Locate every blood parasite and identify its species.
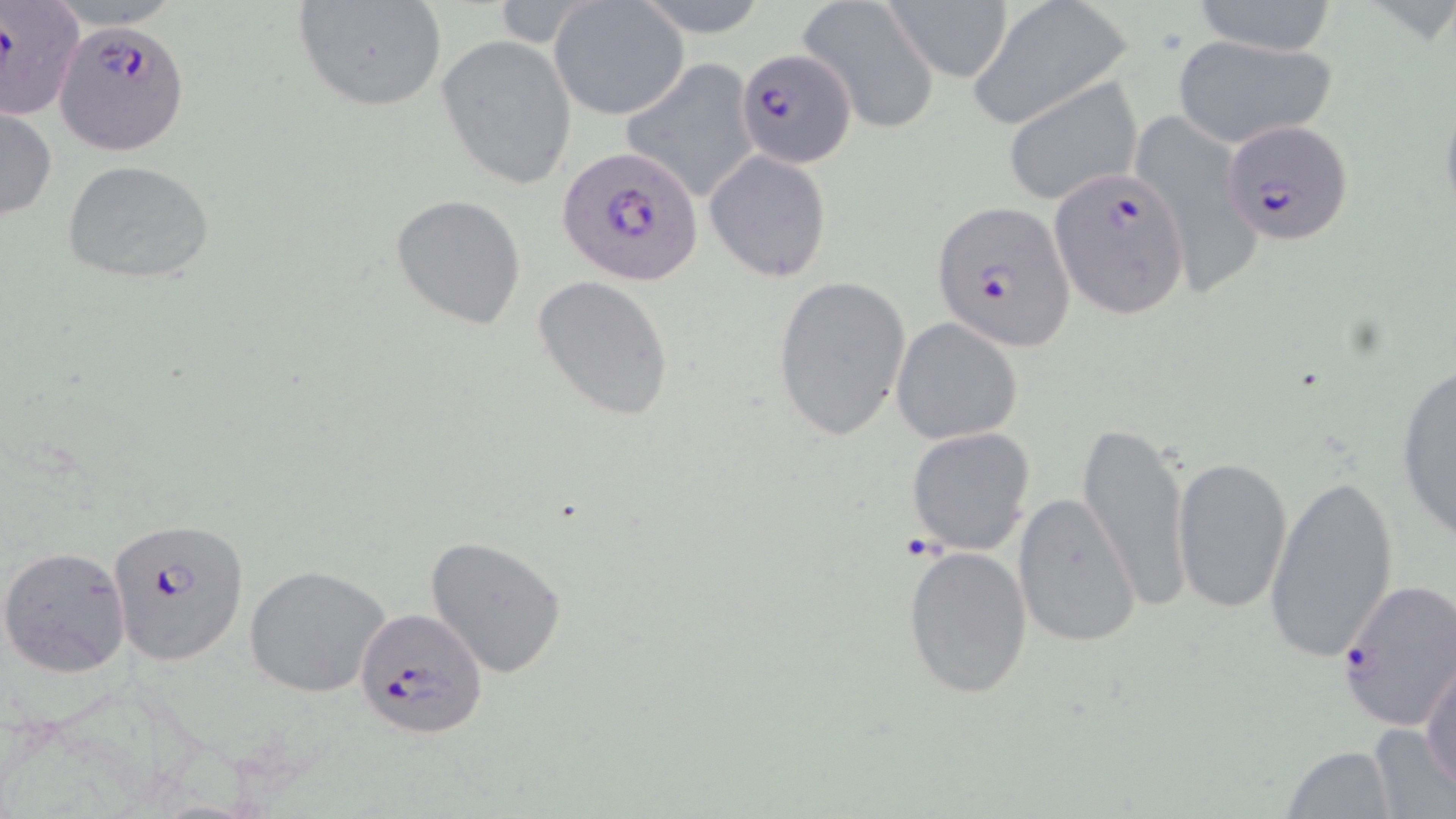

Approximate bounding boxes as (x1,y1)-(x2,y2) corner pairs in pixels.
Plasmodium falciparum-infected red blood cells: (0,3)-(80,121), (54,20)-(190,155), (736,47)-(857,168), (1222,121)-(1355,246), (557,146)-(702,284), (1046,166)-(1189,320), (930,203)-(1075,350), (107,516)-(247,664), (1336,579)-(1456,732), (353,607)-(488,738).
No Plasmodium ovale, Plasmodium malariae, Plasmodium vivax, Babesia divergens, or Trypanosoma brucei observed.

Uninfected red blood cell locations: (292,0)-(449,113), (633,0)-(773,39), (798,0)-(941,134), (883,0)-(1014,83), (549,1)-(687,121), (1187,1)-(1341,56), (972,2)-(1132,124), (438,33)-(576,189), (1171,35)-(1338,148), (621,57)-(760,203), (1001,77)-(1144,206), (0,105)-(56,222), (1125,107)-(1265,291), (703,150)-(834,284), (62,158)-(215,285), (390,193)-(527,330), (772,274)-(912,441), (534,275)-(675,420), (889,317)-(1024,445), (1394,359)-(1456,544), (1077,421)-(1192,611), (906,428)-(1036,555), (1171,455)-(1292,614), (1265,472)-(1398,662), (1012,491)-(1142,649), (425,535)-(568,679), (903,544)-(1033,699), (0,545)-(131,678), (244,564)-(393,700), (1420,653)-(1456,792), (1366,723)-(1453,818), (1283,743)-(1397,818). Slide-level diagnosis: Plasmodium falciparum. 1000x magnification. Light microscopy. May-Grünwald-Giemsa stain. Single field of view. Image is 1456×819 pixels. Thin blood smear.